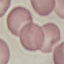

{
  "malaria_status": "uninfected",
  "capture": "smartphone camera at the microscope eyepiece",
  "image_type": "automatically extracted cell patch, resized to 64 × 64 pixels",
  "preparation": "thin smear",
  "stain": "Giemsa"
}